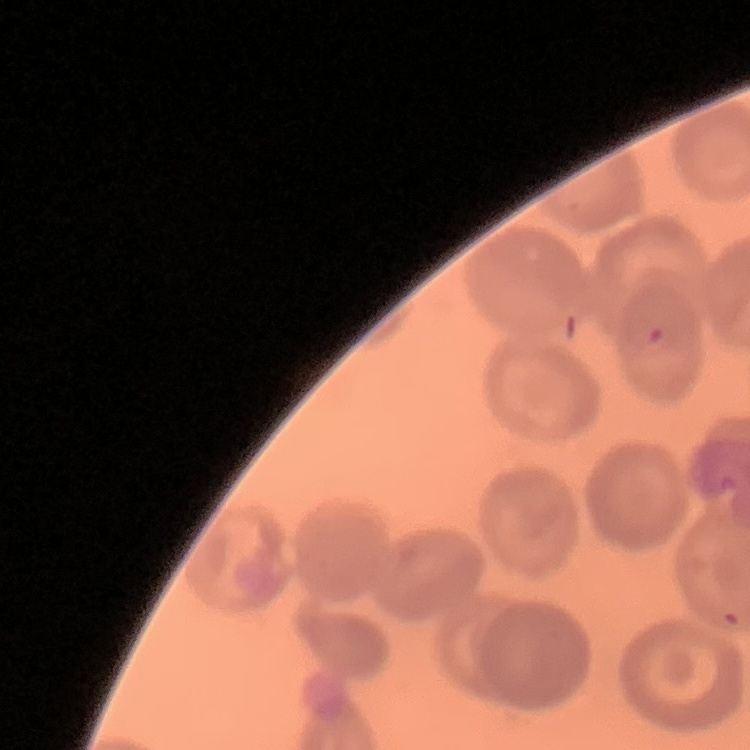
Summary:
  - Erythrocyte morphology: no rouleaux formation
  - Stain: Field's or Giemsa
  - Image type: square crop of a larger photomicrograph
  - Preparation: thin peripheral smear